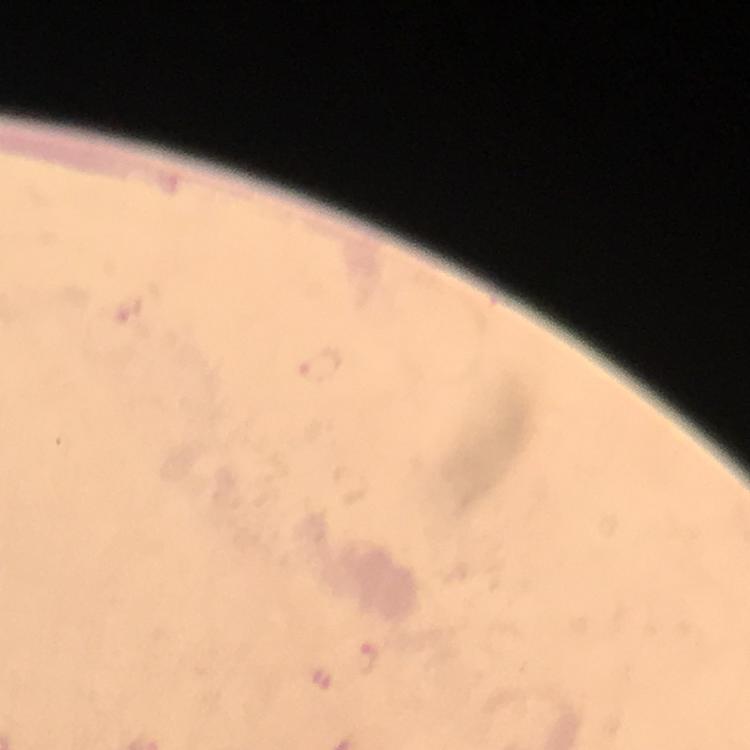

Approximate centers as (x, y) in pixels. Plasmodium parasite locations: (320, 364), (366, 659), (318, 674). Image is 750×750 pixels. Smartphone photograph taken through a microscope. Cropped region of a single field of view. At 100x magnification. Thick blood film. Giemsa stain. Immersion oil was used. From a diagnostic examination for malaria.